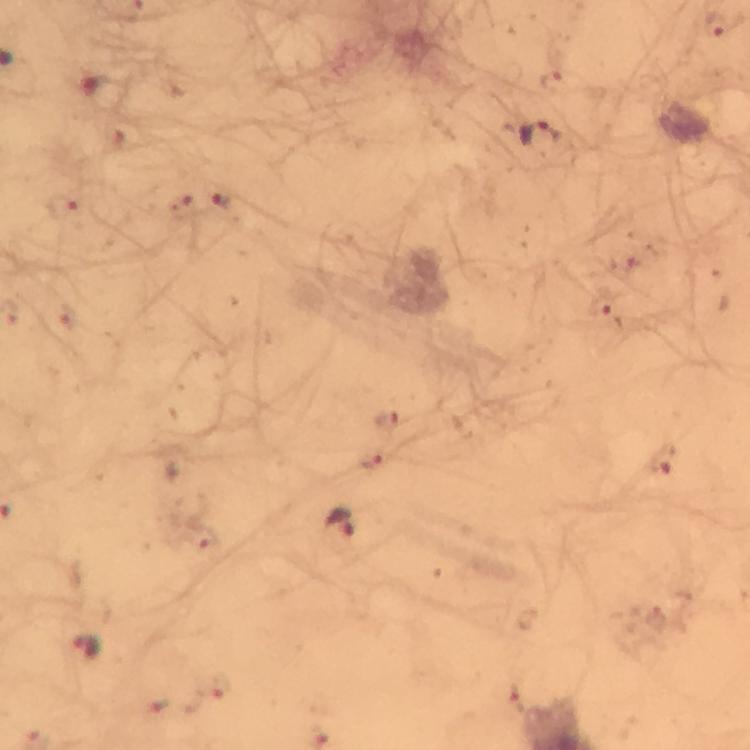
Approximate object centers, in pixels from the top-left corner.
Summary:
  - Plasmodium parasite locations: (x=716, y=24), (x=538, y=135), (x=222, y=200), (x=62, y=205), (x=182, y=207), (x=600, y=303), (x=389, y=421), (x=662, y=460), (x=373, y=461), (x=340, y=523), (x=87, y=646), (x=219, y=687)
  - Immersion oil: applied
  - Magnification: 100x
  - Cropped from: one field of view
  - Image size: 750×750 pixels
  - Context: from a diagnostic examination for malaria
  - Stain: Giemsa
  - Preparation: thick blood film
  - Capture: smartphone camera through the microscope